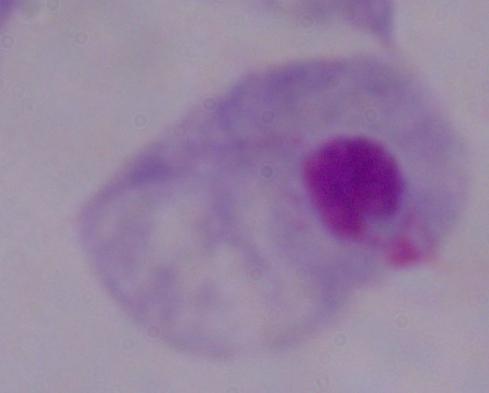

Captured at 1000x magnification. A trichomonad is shown. Micrograph.